State which parasite is depicted.
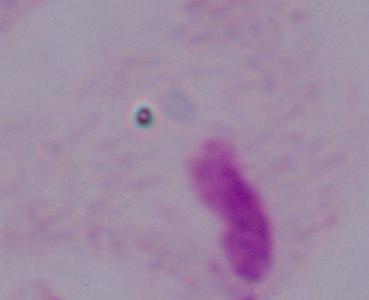

This is a trichomonad.

modality = photomicrograph
magnification = 1000x